State which parasite is depicted.
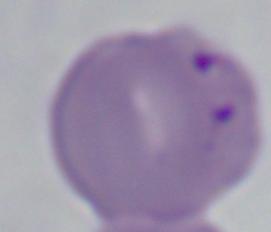
Babesia.

Summary:
  - Magnification: 1000x
  - Modality: photomicrograph